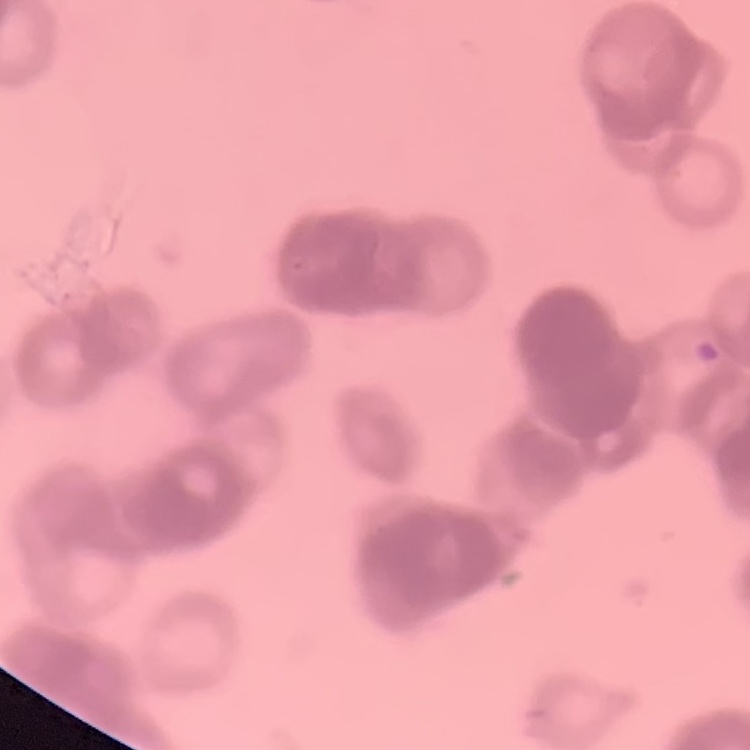 The red blood cells exhibit rouleaux formation. One tile cut from a larger photomicrograph. Thin peripheral smear. Field's or Giemsa stain.